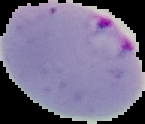

{
  "malaria_status": "parasitized",
  "preparation": "thin blood film",
  "image_type": "cell region segmented out of the field of view; surrounding area masked to black",
  "image_size": "145×124 pixels"
}